Report the malaria status of this cell.
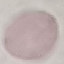
It is uninfected.

Cell patch, automatically extracted from a larger field of view and resized to 64 × 64 pixels. Photographed with a smartphone camera at the microscope eyepiece. Giemsa stain. Thin smear of blood.